Identify the blood parasite species.
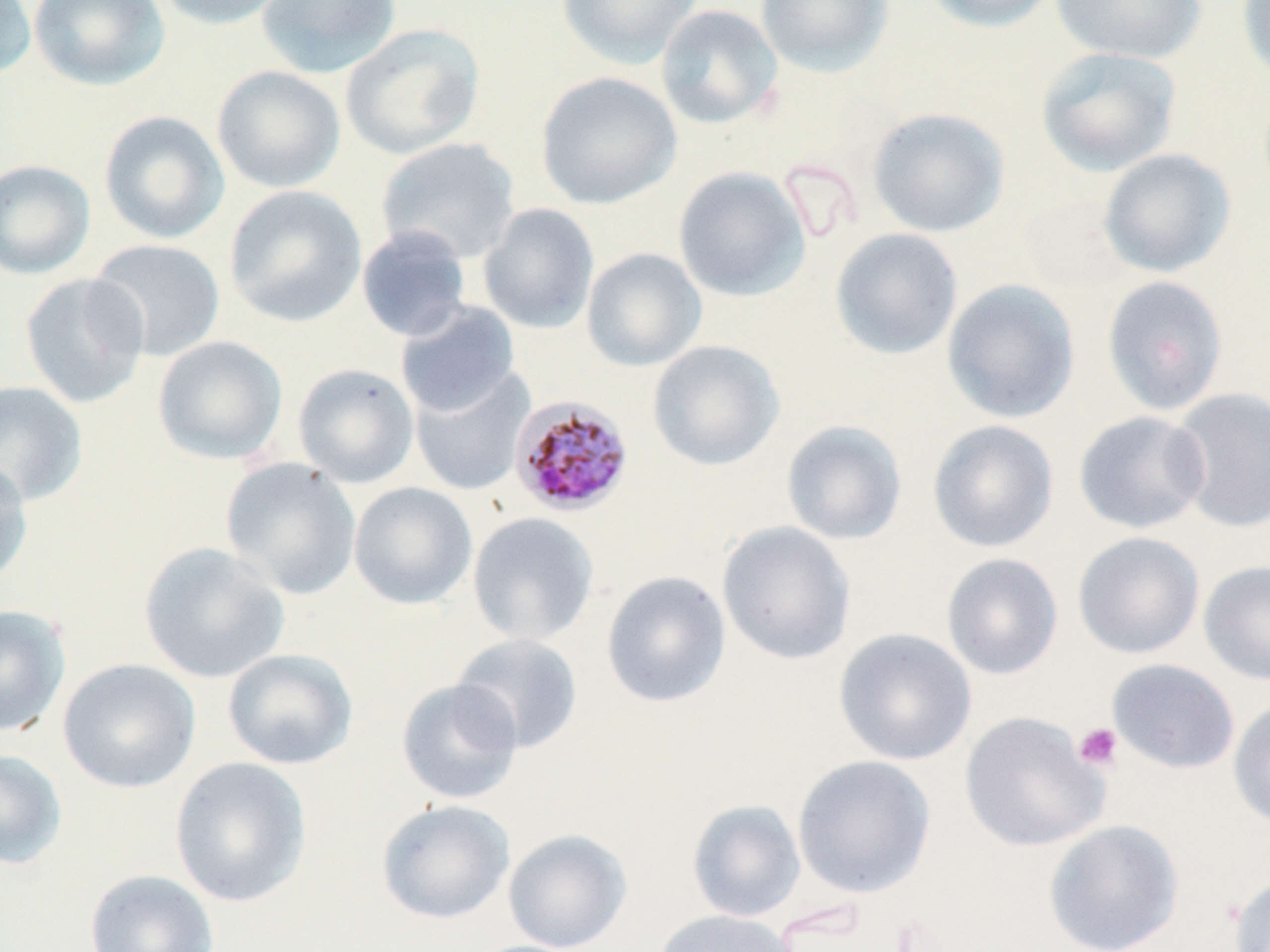
Plasmodium malariae.

Approximate bounding boxes as (x1,y1)-(x2,y2) corner pairs in pixels. Platelet locations: (1073,722)-(1123,771). Plasmodium malariae-infected red blood cell locations: (509,395)-(634,516). Uninfected red blood cell locations: (0,0)-(36,80), (29,0)-(170,90), (151,0)-(290,30), (256,0)-(401,78), (557,0)-(703,70), (755,0)-(894,77), (920,0)-(1061,32), (1050,0)-(1207,64), (1236,0)-(1270,87), (655,4)-(783,129), (340,23)-(486,160), (1035,46)-(1183,178), (212,65)-(346,193), (535,71)-(682,209), (868,107)-(1011,238), (99,110)-(230,245), (376,137)-(521,264), (1098,148)-(1236,277), (0,159)-(96,280), (673,166)-(812,302), (224,185)-(367,328), (1017,193)-(1134,293), (477,203)-(600,334), (352,220)-(603,336), (356,225)-(473,343), (830,228)-(963,360), (88,238)-(226,361), (582,248)-(707,371), (19,272)-(150,409), (1101,275)-(1229,416), (941,279)-(1081,424), (395,301)-(521,417), (152,336)-(288,465), (647,340)-(785,471), (292,363)-(419,489), (409,366)-(534,496), (0,380)-(89,508), (1169,387)-(1270,533), (1073,410)-(1211,534), (927,419)-(1059,553), (781,420)-(907,546), (220,457)-(362,600), (0,460)-(34,587), (348,481)-(478,610), (467,512)-(600,646), (717,521)-(857,665), (1073,531)-(1205,659), (138,542)-(290,684), (941,552)-(1064,680), (1199,559)-(1270,686), (601,570)-(731,708), (0,605)-(71,737), (833,627)-(977,766), (451,633)-(583,753), (221,648)-(358,770), (58,657)-(201,793), (1106,658)-(1240,775), (396,678)-(524,805), (1228,697)-(1270,831), (960,711)-(1108,852), (0,748)-(68,870), (791,754)-(936,899), (170,757)-(312,908), (376,799)-(515,924), (687,799)-(806,922), (1043,818)-(1184,952), (502,827)-(633,952), (84,868)-(220,952), (1227,871)-(1270,952), (651,909)-(802,952). One field of a larger specimen. Optical microscopy. Captured at 1000x magnification. Thin blood film. Image is 1270×952 pixels. May-Grünwald-Giemsa stain.